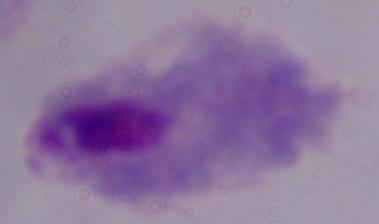

Photomicrograph. 1000x magnification. A trichomonad is shown.